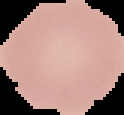
Segmented cell region on a black background. Malaria status: uninfected. Image is 124×115 pixels. From a thin blood smear.